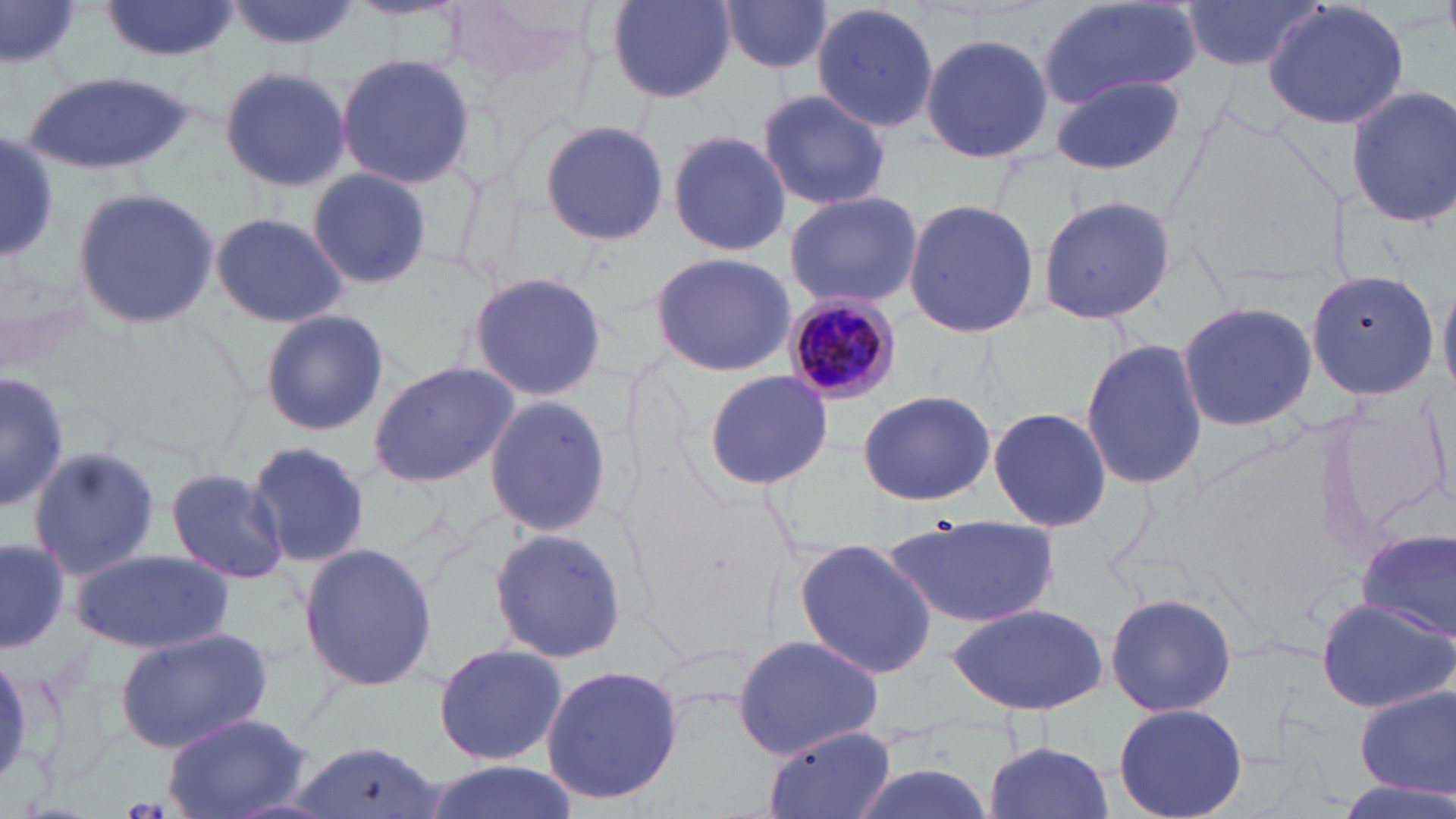
Plasmodium malariae-infected red blood cell locations = approximate bounding boxes as (x1, y1, x2, y2) in pixels: (783, 294, 899, 405)
slide-level diagnosis = Plasmodium malariae
modality = optical microscopy
uninfected red blood cell locations = approximate bounding boxes as (x1, y1, x2, y2) in pixels: (101, 0, 238, 61), (226, 0, 363, 52), (1036, 0, 1202, 111), (1183, 0, 1321, 70), (1263, 0, 1410, 131), (607, 1, 736, 102), (717, 1, 835, 79), (810, 1, 940, 135), (0, 3, 82, 75), (920, 31, 1055, 163), (335, 54, 480, 187), (217, 64, 352, 193), (20, 71, 197, 177), (1050, 74, 1185, 177), (1345, 85, 1456, 230), (758, 88, 892, 210), (538, 119, 669, 247), (667, 128, 792, 258), (0, 136, 61, 261), (305, 168, 435, 287), (71, 185, 223, 331), (782, 190, 922, 310), (1038, 192, 1175, 326), (902, 197, 1042, 338), (208, 212, 352, 327), (651, 250, 796, 377), (1306, 269, 1437, 400), (466, 271, 609, 401), (1439, 280, 1455, 403), (1175, 301, 1319, 432), (259, 310, 391, 436), (1080, 336, 1208, 492), (367, 359, 520, 490), (0, 370, 69, 513), (702, 370, 834, 491), (857, 389, 995, 504), (482, 394, 614, 538), (987, 405, 1111, 534), (247, 440, 372, 570), (26, 446, 162, 580), (164, 465, 290, 585), (882, 517, 1059, 629), (487, 527, 626, 664), (1353, 531, 1456, 637), (792, 536, 940, 676), (0, 538, 68, 655), (298, 543, 440, 693), (73, 549, 234, 654), (1104, 592, 1239, 718), (1314, 595, 1455, 715), (943, 603, 1111, 715), (114, 627, 273, 754), (730, 635, 886, 759), (432, 642, 568, 764), (538, 664, 685, 807), (1352, 688, 1456, 799), (1113, 702, 1248, 819), (161, 713, 311, 819), (764, 726, 898, 819), (982, 739, 1116, 819), (287, 740, 449, 818), (415, 761, 580, 819), (840, 761, 1001, 819), (1332, 777, 1456, 819)
image size = 1456×819 pixels
preparation = thin blood film
magnification = 1000x
field of view = one of a larger specimen
stain = May-Grünwald-Giemsa